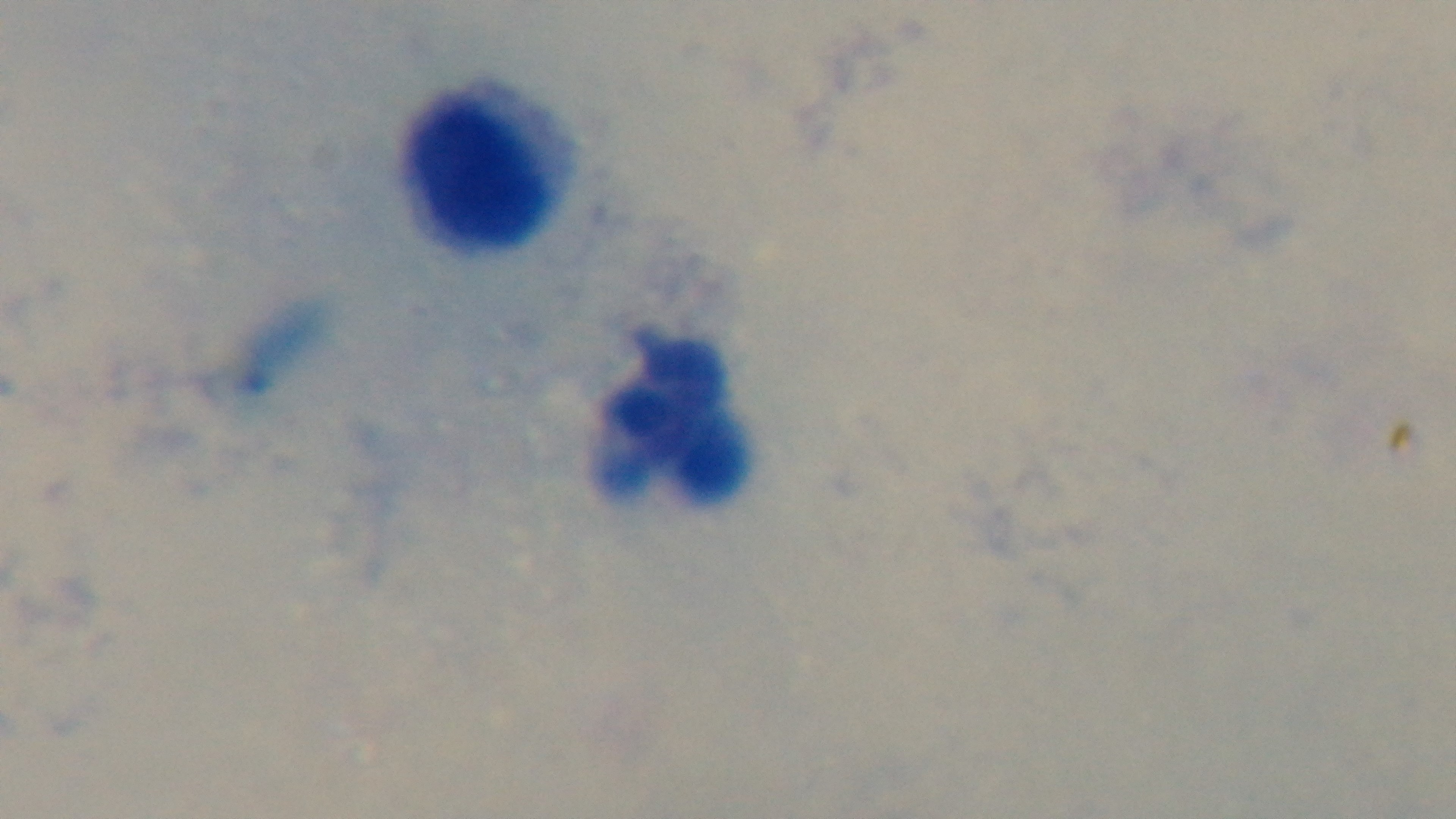

Malaria status: uninfected. Mounted 4K digital camera. One field from the slide. Preparation: thick blood film. Oil-immersion objective, 100x. Giemsa stain. Light microscopy.